Comment on the morphology of the erythrocytes.
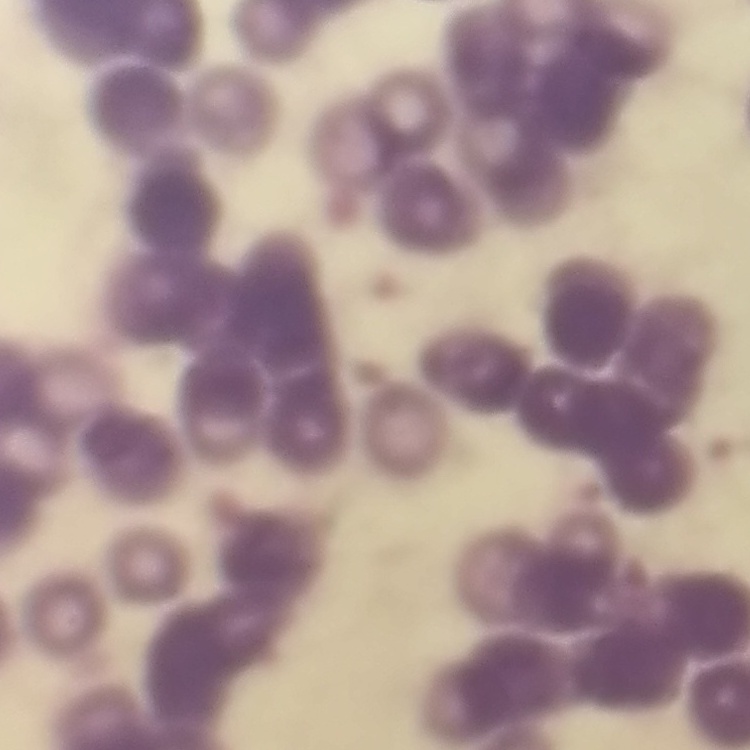

They show rouleaux formation.

Field's or Giemsa stain. Thin blood smear. Square crop of a larger photomicrograph.